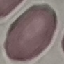

result = no malaria parasites detected
preparation = thin blood film
stain = Giemsa
image type = cell patch, automatically extracted from a larger field of view and resized to 64 × 64 pixels
capture = smartphone camera at the microscope eyepiece